Report the malaria status of this cell.
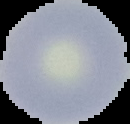
Uninfected.

preparation = thin blood film
image type = segmented cell region on a black background
image size = 130×124 pixels